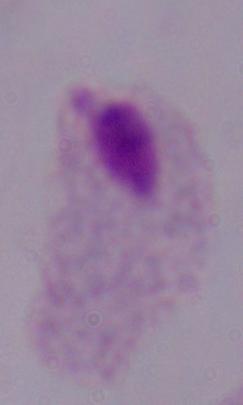
Photomicrograph. A trichomonad is shown. 1000x magnification.